Identify the cell.
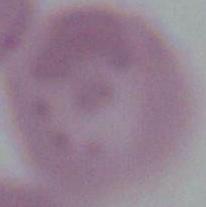

An erythrocyte.

magnification = 1000x
modality = photomicrograph